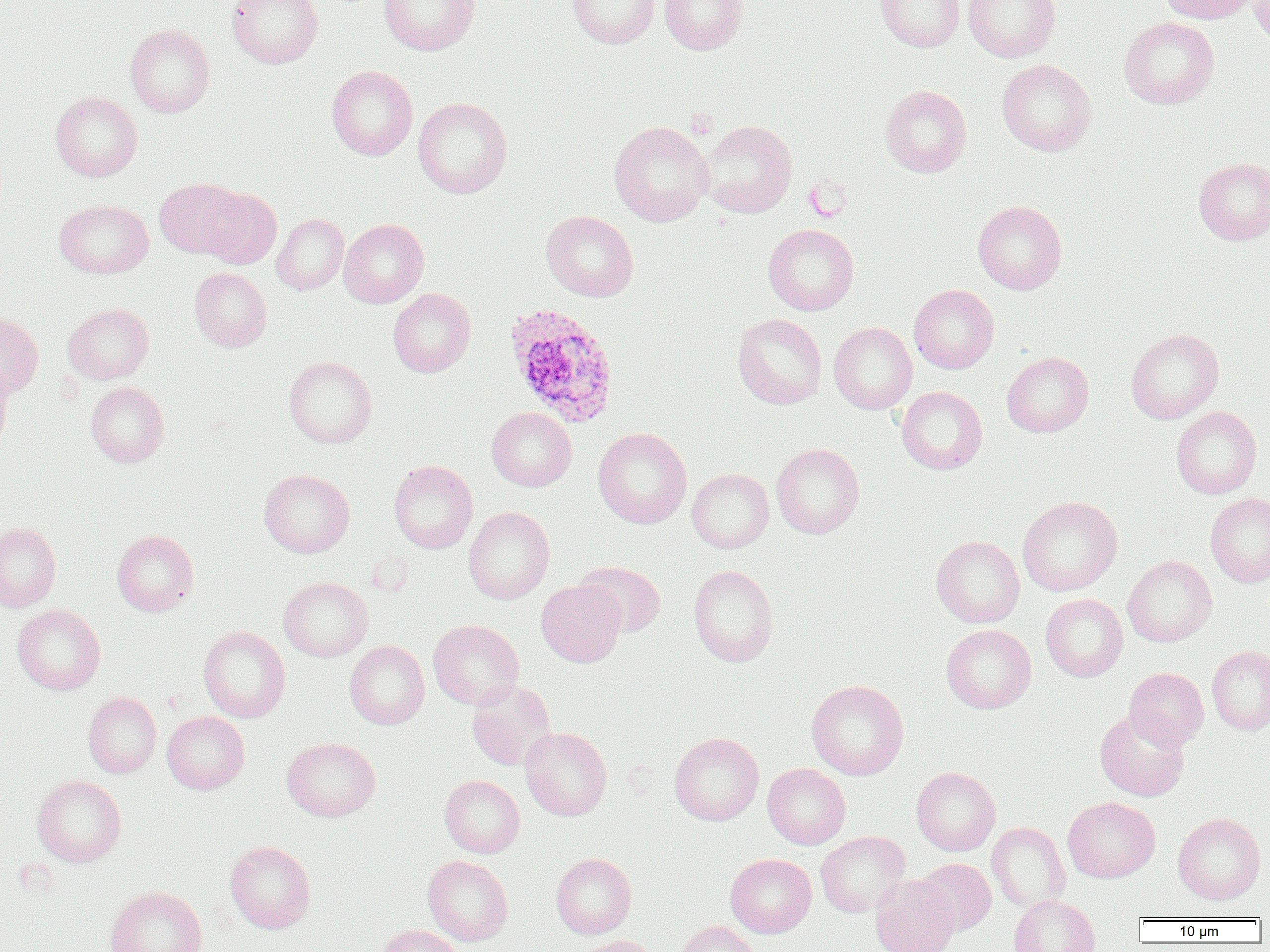
Summary:
  - Coordinate format: approximate bounding boxes as [x1, y1, x2, y2] in pixels
  - Uninfected red blood cell locations: [227, 0, 323, 68], [379, 0, 479, 55], [567, 0, 660, 48], [659, 0, 747, 54], [876, 0, 964, 52], [963, 0, 1060, 62], [1156, 0, 1257, 24], [1249, 0, 1270, 50], [1119, 16, 1219, 109], [125, 24, 215, 117], [997, 59, 1096, 156], [326, 65, 417, 160], [879, 84, 972, 178], [50, 91, 142, 181], [413, 97, 512, 199], [700, 120, 797, 218], [609, 121, 714, 227], [1193, 157, 1270, 245], [155, 177, 248, 259], [199, 186, 281, 268], [54, 199, 154, 278], [973, 201, 1067, 294], [541, 210, 638, 302], [272, 213, 349, 295], [338, 219, 428, 308], [763, 224, 859, 315], [189, 268, 272, 352], [909, 284, 999, 374], [388, 288, 476, 377], [63, 303, 154, 383], [0, 311, 43, 398], [733, 313, 827, 409], [829, 322, 917, 414], [1125, 328, 1224, 424], [1002, 351, 1093, 437], [283, 356, 377, 448], [0, 364, 14, 450], [86, 381, 169, 467], [896, 386, 987, 475], [1171, 406, 1262, 499], [486, 407, 577, 491], [593, 427, 692, 528], [771, 443, 865, 539], [389, 460, 478, 553], [687, 468, 774, 553], [258, 469, 355, 558], [1205, 492, 1270, 587], [1017, 496, 1123, 596], [463, 506, 554, 604], [0, 522, 61, 612], [112, 529, 199, 616], [931, 535, 1025, 627], [1123, 555, 1217, 646], [573, 561, 666, 637], [688, 564, 779, 667], [278, 577, 373, 662], [536, 580, 626, 667], [1040, 594, 1128, 682], [12, 604, 105, 695], [428, 619, 524, 709], [941, 624, 1036, 713], [198, 625, 290, 723], [344, 640, 430, 729], [1207, 645, 1270, 735], [1124, 667, 1209, 750], [806, 679, 909, 780], [467, 680, 556, 770], [83, 691, 162, 778], [1094, 708, 1190, 802], [162, 711, 249, 794], [520, 727, 612, 821], [669, 732, 764, 826], [282, 737, 381, 822], [762, 763, 850, 849], [911, 766, 1000, 856], [32, 775, 126, 867], [439, 775, 524, 858], [1063, 797, 1160, 883], [1172, 812, 1266, 904], [987, 822, 1070, 911], [816, 831, 910, 917], [225, 840, 315, 933], [551, 852, 637, 939], [725, 853, 817, 937], [423, 855, 513, 945], [916, 858, 996, 936], [870, 875, 959, 952], [105, 886, 207, 952], [1009, 895, 1099, 952], [673, 921, 762, 952], [376, 924, 462, 952], [572, 936, 660, 952]
  - Plasmodium ovale-infected red blood cell locations: [504, 303, 619, 428]
  - Slide-level diagnosis: Plasmodium ovale
  - Modality: light microscopy
  - Field of view: one of a larger specimen
  - Image size: 1270×952 pixels
  - Preparation: thin blood smear
  - Magnification: 1000x